Identify the parasite.
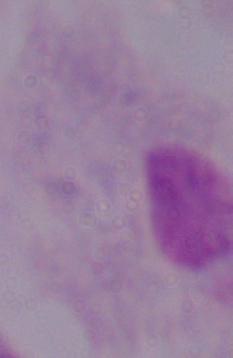

A trichomonad.

1000x magnification. Micrograph.